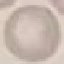
Summary:
  - Malaria status: uninfected
  - Capture: smartphone through the microscope eyepiece
  - Image type: automatically extracted cell patch, resized to 64 × 64 pixels
  - Stain: Giemsa
  - Preparation: thin blood smear